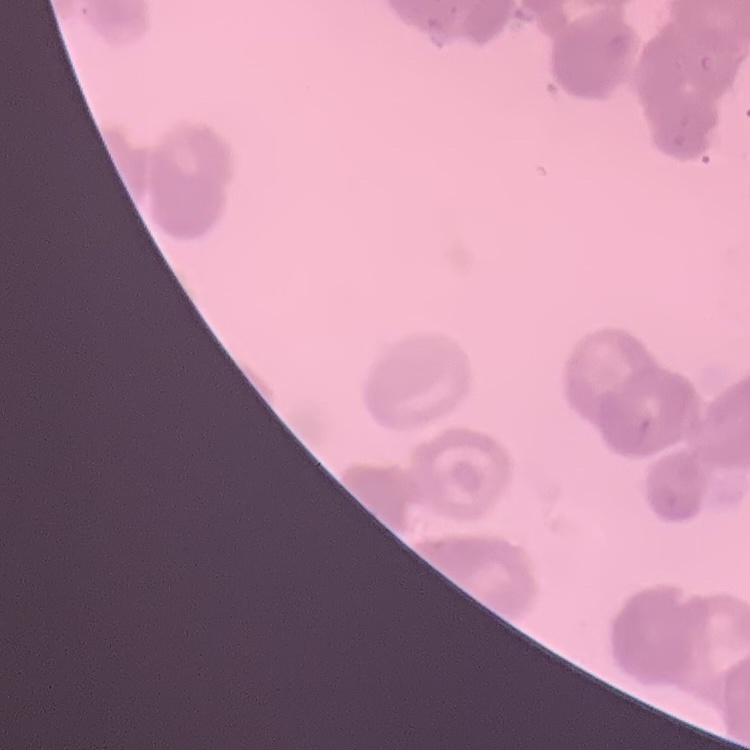 The red blood cells exhibit rouleaux formation. Field's or Giemsa stain. One tile cut from a larger photomicrograph. Thin blood smear.